Name the parasite shown.
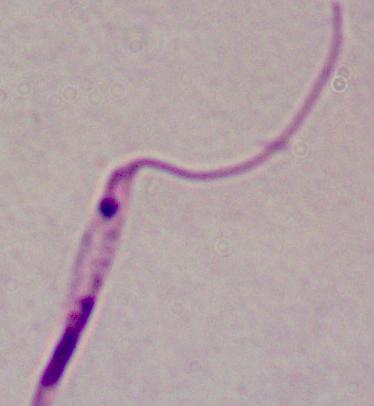
This is Leishmania.

Captured at 1000x magnification. Micrograph.